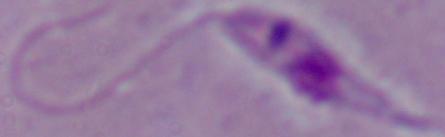
Summary:
  - Magnification: 1000x
  - Identification: Leishmania
  - Modality: micrograph